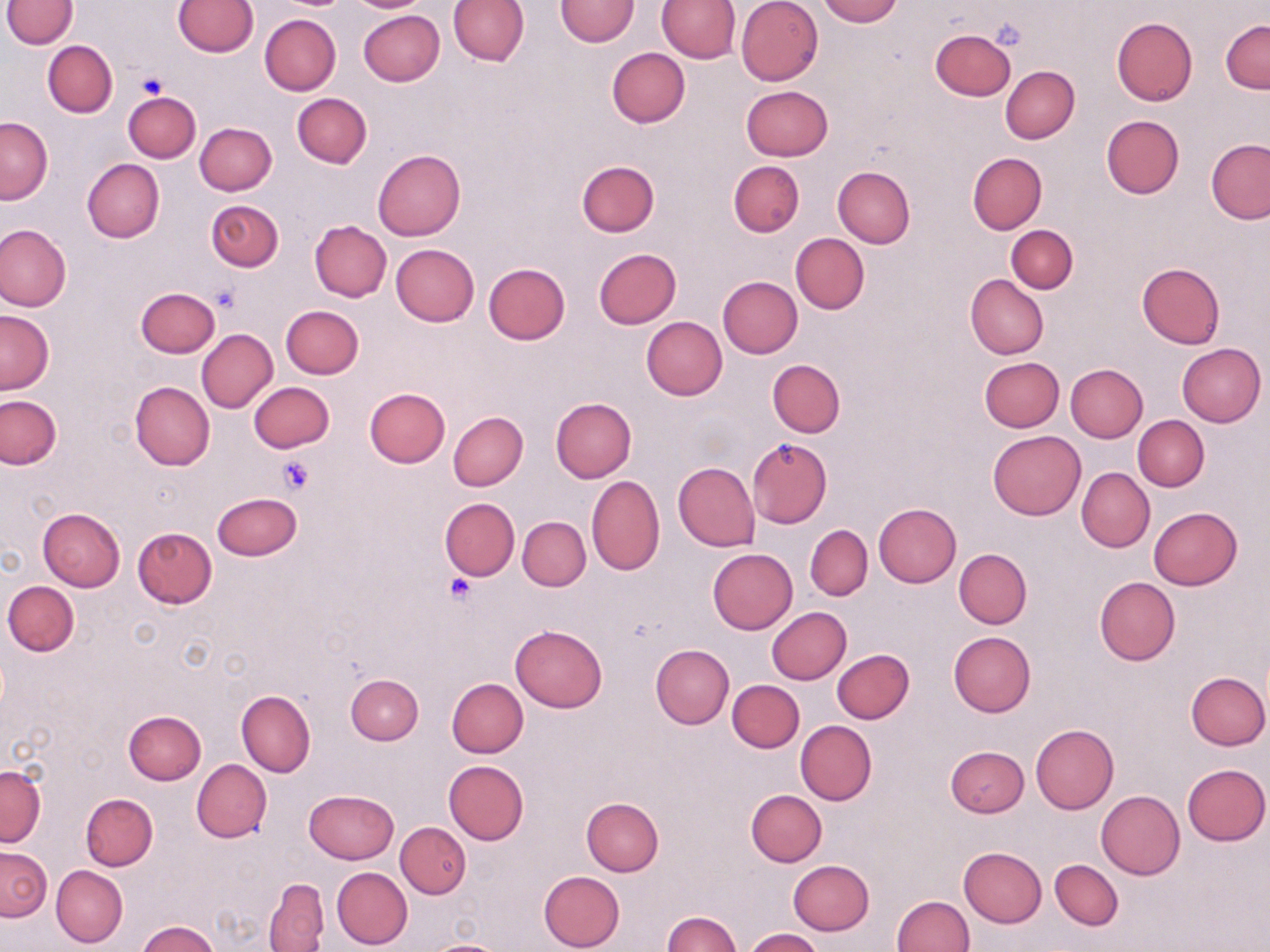

Summary:
  - Coordinate format: approximate bounding boxes as (x1,y1)-(x2,y2) corner pairs in pixels
  - Platelet locations: (138,70)-(169,99), (210,286)-(240,315), (278,457)-(313,494), (444,571)-(480,604)
  - Uninfected red blood cell locations: (3,0)-(77,48), (173,0)-(258,57), (278,0)-(349,9), (345,0)-(433,13), (448,0)-(528,66), (554,0)-(639,46), (736,0)-(824,85), (818,0)-(900,26), (657,1)-(741,63), (357,10)-(444,87), (259,14)-(340,95), (1112,18)-(1197,105), (1220,20)-(1269,94), (929,28)-(1015,101), (43,39)-(117,117), (607,48)-(689,127), (1000,65)-(1080,144), (739,85)-(819,235), (741,85)-(834,160), (124,91)-(201,163), (292,93)-(371,168), (1101,114)-(1184,199), (1,117)-(52,203), (195,121)-(277,195), (1205,139)-(1270,224), (373,149)-(465,241), (968,153)-(1047,233), (81,159)-(164,243), (576,160)-(659,237), (728,160)-(804,237), (833,166)-(915,248), (206,199)-(283,272), (309,220)-(392,301), (0,224)-(72,311), (1006,225)-(1078,293), (791,233)-(869,314), (390,243)-(478,327), (593,249)-(681,328), (1137,263)-(1224,348), (483,264)-(569,345), (964,274)-(1047,360), (718,275)-(802,358), (136,287)-(220,358), (281,305)-(364,379), (1,310)-(54,394), (640,316)-(727,400), (196,329)-(277,413), (1176,343)-(1266,427), (979,356)-(1064,432), (769,359)-(845,437), (1066,364)-(1148,442), (130,381)-(214,470), (248,381)-(334,453), (364,387)-(451,468), (0,395)-(61,469), (549,397)-(636,482), (448,412)-(527,490), (1133,415)-(1209,491), (987,431)-(1085,520), (746,436)-(832,528), (673,462)-(760,551), (1076,467)-(1154,553), (587,475)-(665,576), (212,492)-(302,561), (439,497)-(520,580), (873,502)-(961,587), (1148,507)-(1242,590), (38,508)-(126,591), (518,515)-(590,591), (805,525)-(873,600), (132,527)-(218,608), (707,547)-(797,634), (954,548)-(1032,629), (1094,576)-(1180,665), (3,580)-(79,657), (767,607)-(851,684), (510,624)-(607,711), (948,631)-(1035,716), (650,644)-(734,729), (831,650)-(913,724), (1186,671)-(1269,749), (346,674)-(423,744), (447,678)-(528,757), (727,680)-(804,753), (236,689)-(315,778), (123,710)-(206,784), (795,721)-(877,806), (1030,724)-(1119,812), (945,745)-(1029,818), (192,759)-(272,842), (444,760)-(529,844), (0,764)-(45,845), (1181,764)-(1269,846), (304,789)-(397,865), (746,790)-(826,867), (1095,791)-(1185,880), (81,793)-(158,871), (582,797)-(664,875), (396,822)-(471,899), (1,846)-(51,920), (960,847)-(1047,927), (1050,858)-(1123,930), (787,859)-(874,935), (51,865)-(127,948), (331,866)-(412,949), (538,870)-(625,952), (264,879)-(328,950), (892,894)-(973,951), (662,910)-(741,951), (138,921)-(219,952), (743,928)-(823,952), (423,938)-(510,952)
  - Slide-level diagnosis: negative for blood parasites
  - Field of view: one of a larger specimen
  - Modality: light microscopy
  - Preparation: thin blood film
  - Image size: 1270×952 pixels
  - Magnification: 1000x
  - Stain: May-Grünwald-Giemsa